Locate every Plasmodium parasite.
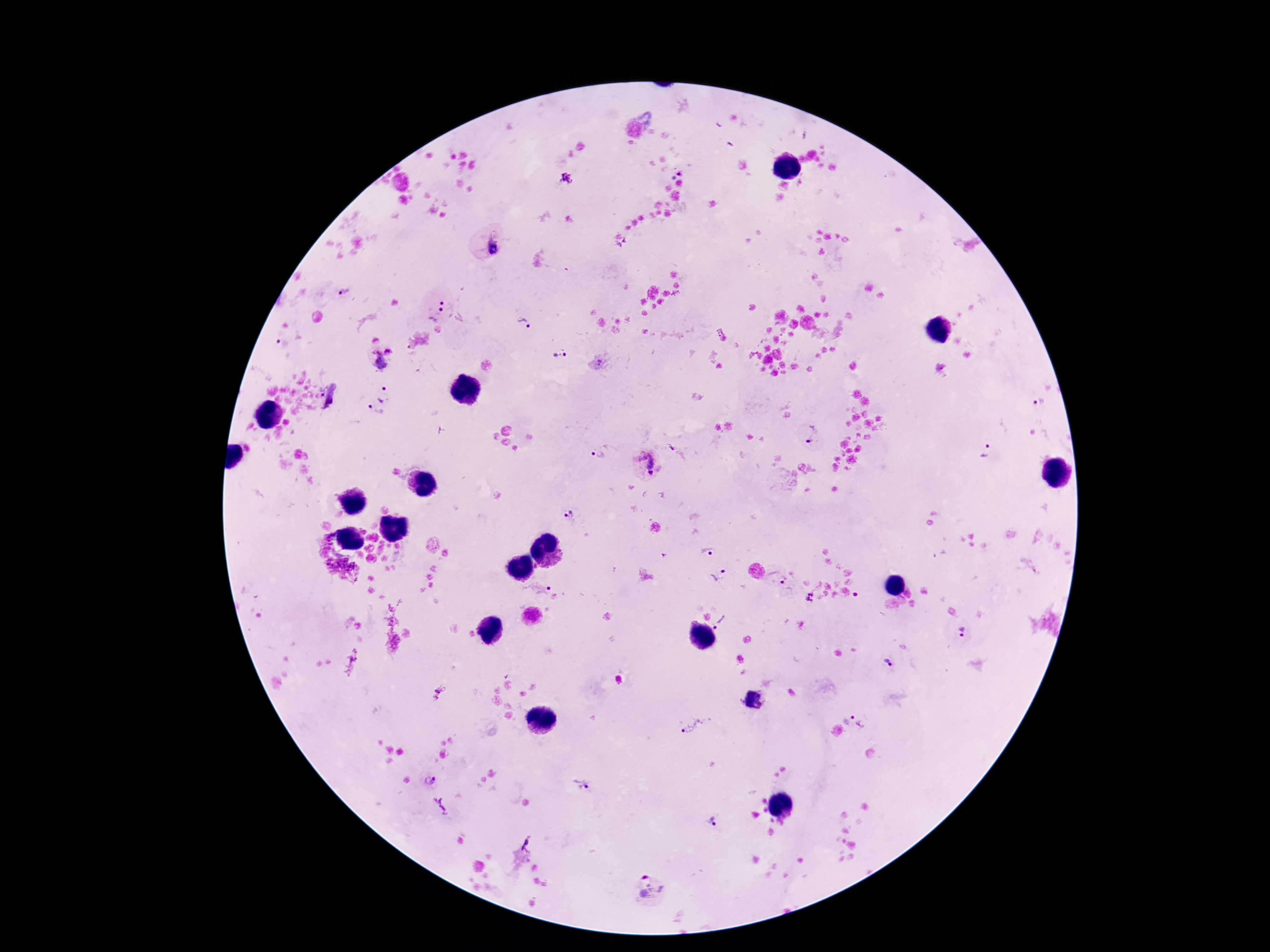

Approximate object centers, in pixels from the top-left corner.
Plasmodium parasites: (x=675, y=170), (x=565, y=178), (x=492, y=247), (x=343, y=294), (x=449, y=302), (x=435, y=313), (x=523, y=324), (x=376, y=340), (x=283, y=343), (x=389, y=349), (x=562, y=355), (x=378, y=359), (x=384, y=393), (x=334, y=395), (x=1041, y=401), (x=375, y=412), (x=812, y=434), (x=671, y=446), (x=987, y=453), (x=599, y=454), (x=648, y=464), (x=569, y=516), (x=709, y=552), (x=719, y=574), (x=778, y=579), (x=539, y=588), (x=723, y=623), (x=963, y=634), (x=888, y=665), (x=437, y=693), (x=859, y=716), (x=695, y=726), (x=429, y=781), (x=583, y=781), (x=712, y=820), (x=527, y=843), (x=651, y=888).

Summary:
  - Capture: smartphone camera through the microscope eyepiece
  - Stain: Giemsa
  - Magnification: 100x
  - Patient malaria status: infected
  - Image size: 1270×952 pixels
  - Preparation: thick blood film
  - Field of view: one from this slide